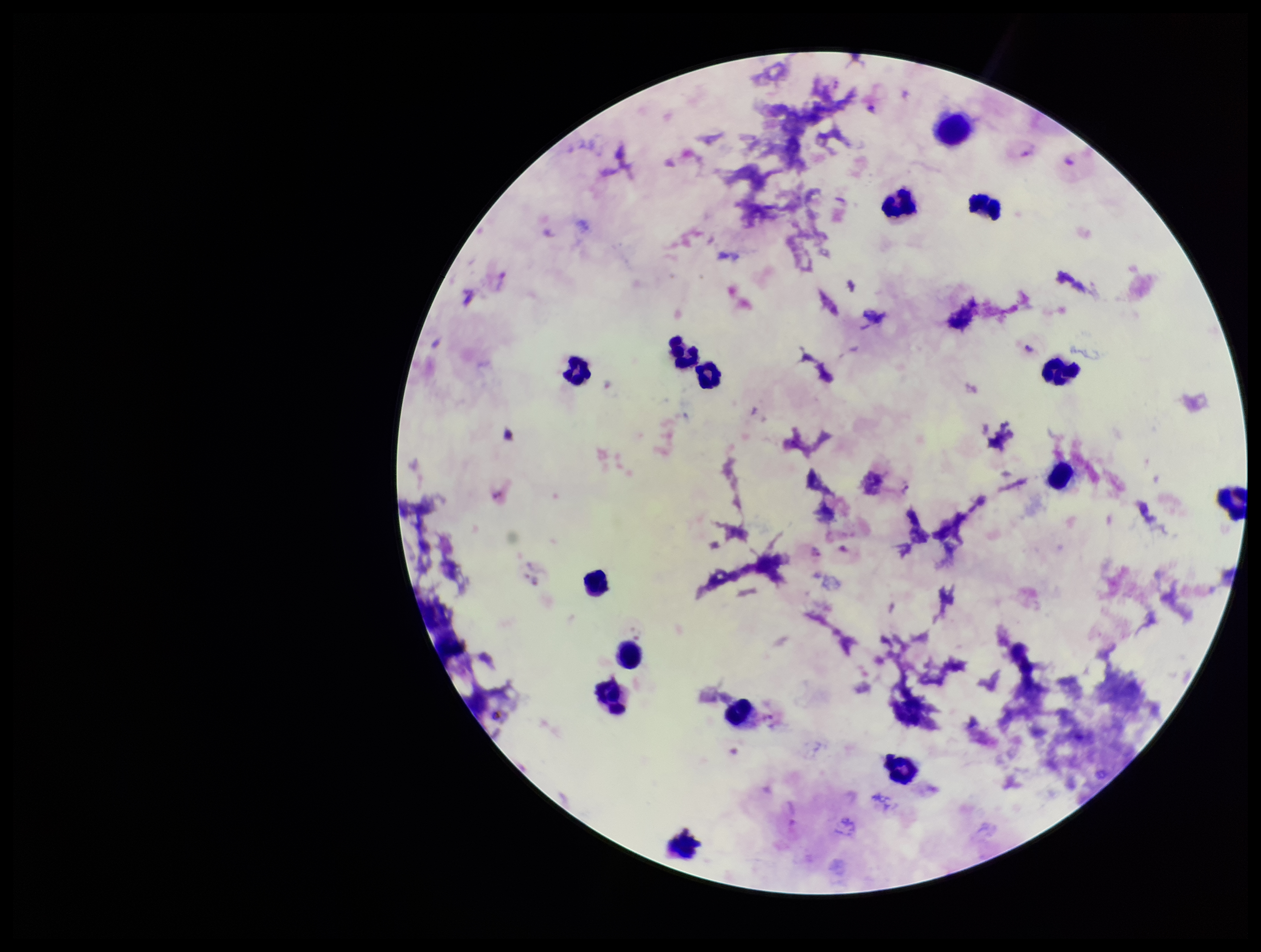

{
  "species_reported_for_this_patient": "Plasmodium vivax",
  "field_of_view": "single",
  "parasite_count": 2,
  "plasmodium_parasites": "seen",
  "image_size": "1261×952 pixels",
  "preparation": "thick blood smear",
  "capture": "smartphone photograph through the microscope eyepiece",
  "leukocyte_count": 16,
  "stain": "Giemsa",
  "patient_malaria_status": "positive"
}